Evaluate for parasitized red blood cells.
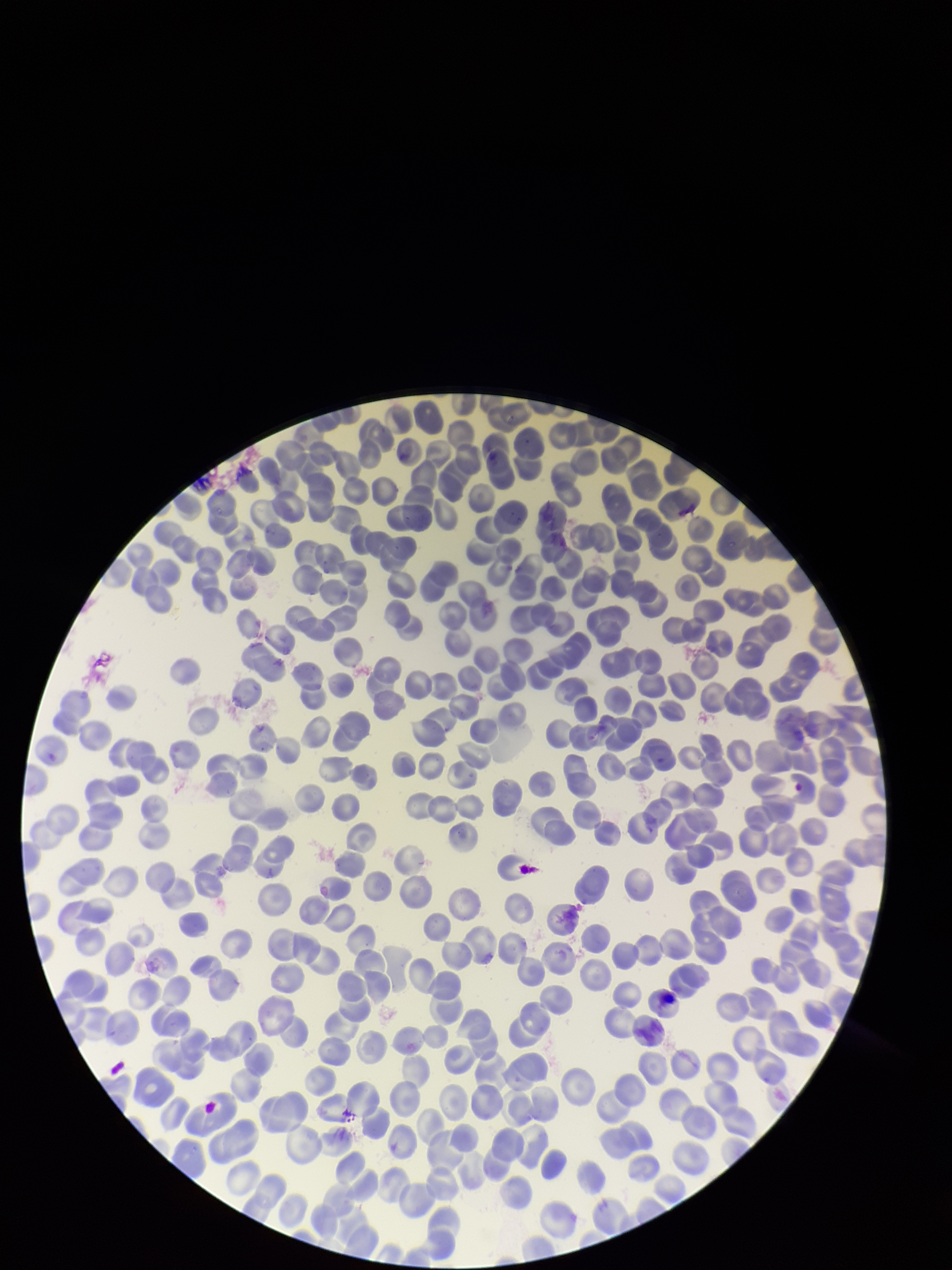

None seen.

Summary:
  - Preparation: thin blood smear
  - Image size: 952×1270 pixels
  - Stain: Giemsa
  - Red blood cell count: 299
  - Field of view: one from this slide
  - Patient malaria status: negative
  - Capture: smartphone photograph through the microscope eyepiece
  - Parasitized red blood cell count: 0